Report the malaria status of this cell.
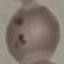
Parasitized.

preparation = thin smear
stain = Giemsa
image type = automatically extracted cell patch, resized to 64 × 64 pixels
capture = smartphone through the microscope eyepiece